Identify the parasite.
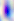
This is Toxoplasma gondii.

Captured at 400x magnification. Micrograph.